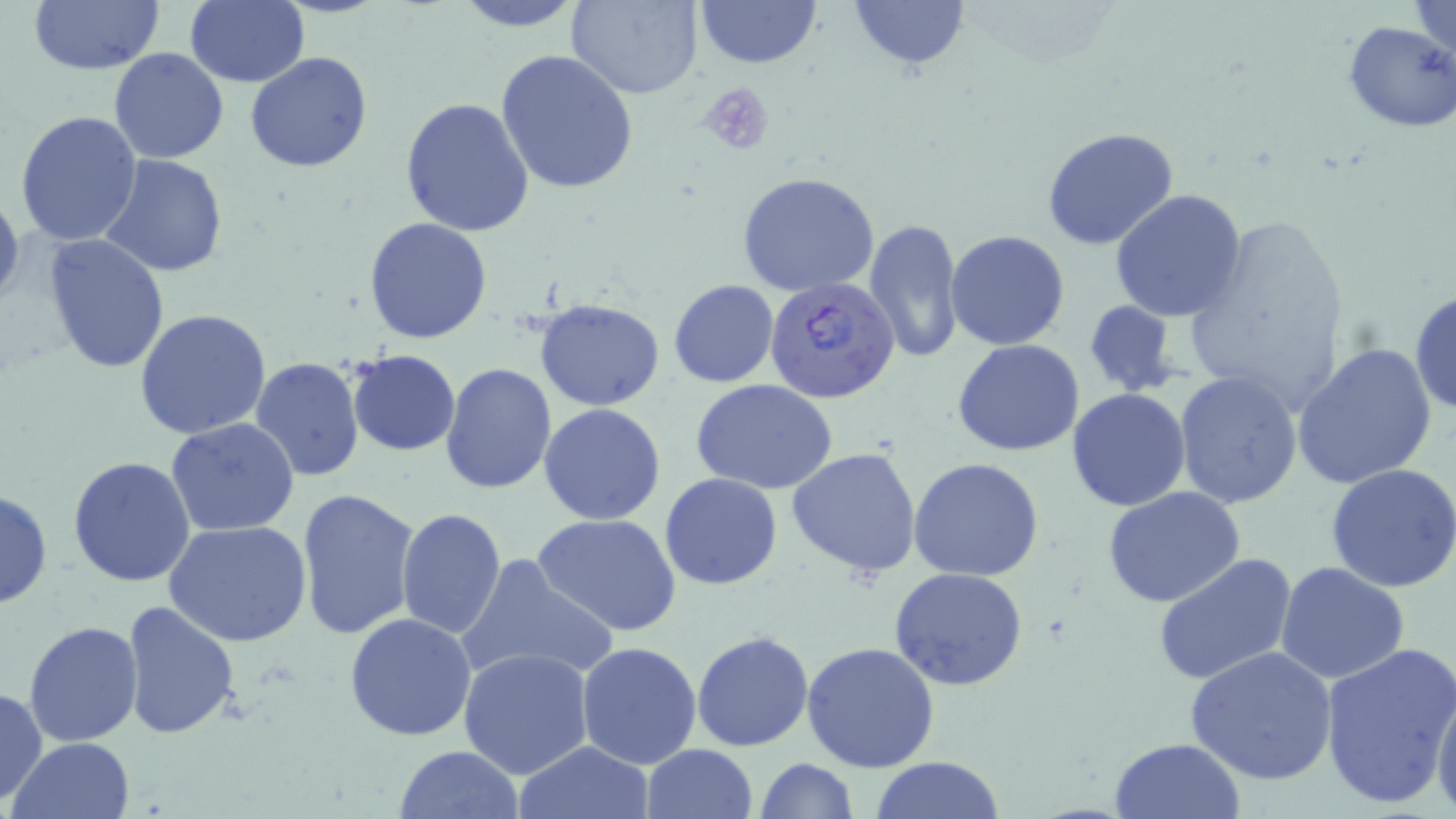

{
  "slide_level_diagnosis": "Plasmodium falciparum",
  "field_of_view": "single",
  "stain": "May-Grünwald-Giemsa",
  "uninfected_red_blood_cell_locations": "approximate bounding boxes as (x1, y1, x2, y2) in pixels: (185, 0, 309, 87), (449, 0, 588, 33), (568, 0, 704, 99), (691, 0, 823, 70), (847, 0, 970, 71), (1409, 0, 1456, 57), (27, 1, 165, 76), (1342, 19, 1456, 133), (108, 48, 230, 164), (495, 49, 638, 195), (245, 51, 373, 173), (400, 97, 535, 236), (14, 111, 143, 247), (1040, 127, 1179, 250), (99, 154, 228, 277), (736, 170, 882, 297), (1110, 190, 1246, 323), (364, 217, 493, 342), (1179, 217, 1352, 414), (864, 218, 965, 365), (945, 230, 1070, 350), (42, 234, 169, 375), (669, 280, 779, 387), (1409, 288, 1455, 417), (535, 298, 665, 412), (1082, 300, 1186, 399), (135, 308, 272, 439), (953, 340, 1085, 456), (1292, 343, 1437, 489), (347, 350, 460, 457), (249, 356, 365, 484), (440, 363, 556, 494), (1174, 371, 1305, 509), (691, 380, 841, 495), (1066, 388, 1193, 512), (539, 403, 666, 526), (167, 418, 299, 536), (787, 446, 924, 578), (66, 456, 196, 588), (908, 457, 1044, 582), (1326, 462, 1456, 592), (660, 473, 783, 590), (1103, 485, 1246, 608), (0, 487, 52, 610), (296, 488, 420, 640), (395, 508, 506, 641), (533, 514, 681, 639), (167, 521, 312, 647), (1151, 553, 1298, 687), (454, 554, 619, 689), (1276, 561, 1410, 685), (888, 567, 1031, 692), (118, 599, 239, 742), (344, 613, 477, 740), (24, 620, 144, 747), (691, 630, 813, 751), (576, 641, 705, 770), (802, 641, 940, 775), (1318, 641, 1456, 807), (1185, 645, 1337, 785), (459, 646, 595, 779), (0, 686, 48, 805), (1431, 686, 1456, 815), (10, 737, 133, 819), (1108, 737, 1245, 818), (512, 740, 656, 819), (641, 743, 758, 819), (394, 745, 524, 819), (869, 756, 1008, 818), (753, 758, 858, 818)",
  "plasmodium_falciparum_infected_red_blood_cell_locations": "approximate bounding boxes as (x1, y1, x2, y2) in pixels: (765, 278, 899, 404)",
  "modality": "light microscopy",
  "magnification": "1000x",
  "platelet_locations": "approximate bounding boxes as (x1, y1, x2, y2) in pixels: (696, 80, 777, 158)",
  "preparation": "thin blood smear",
  "image_size": "1456×819 pixels"
}